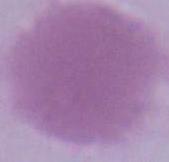
{
  "modality": "photomicrograph",
  "identification": "red blood cell",
  "magnification": "1000x"
}